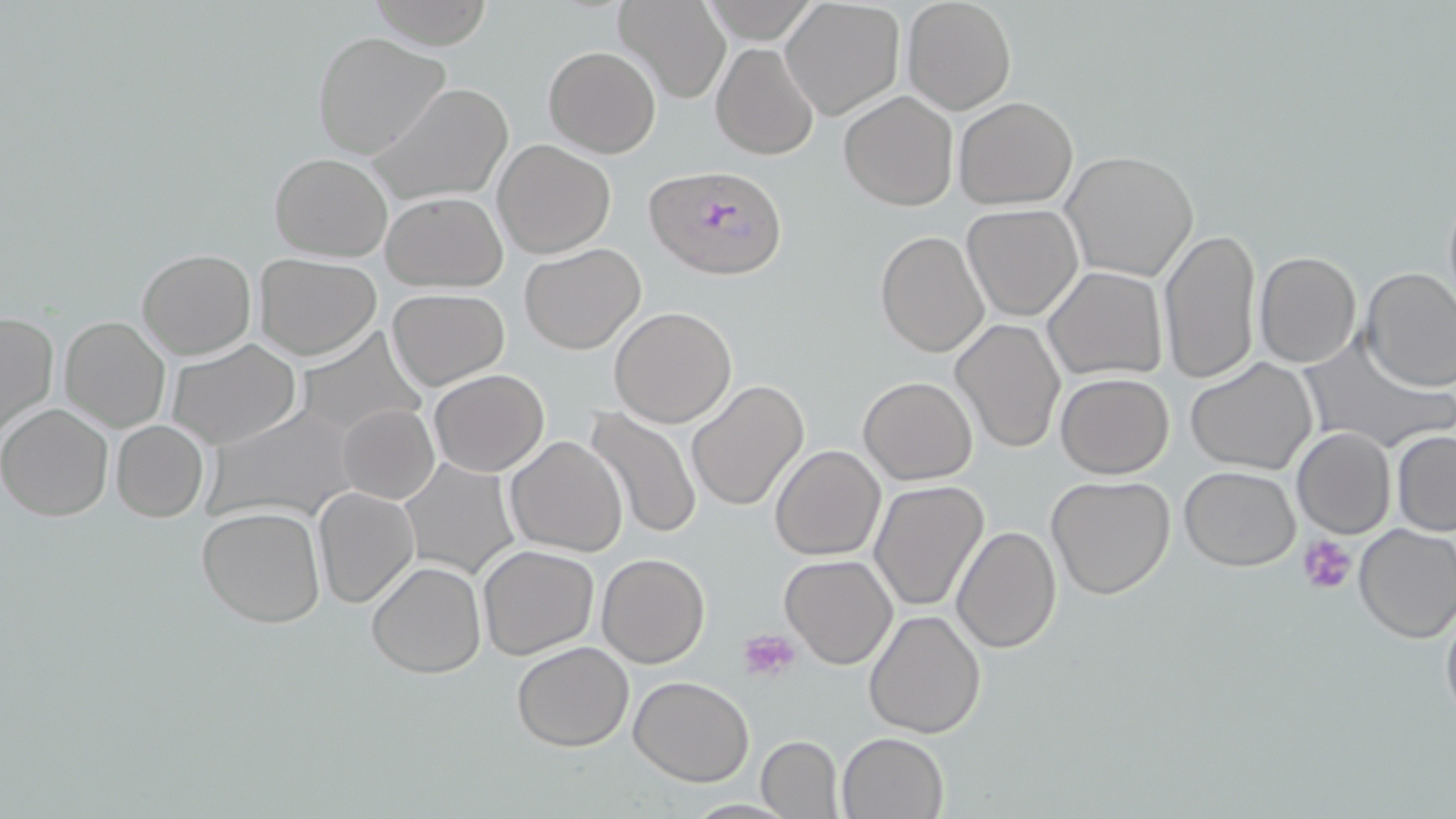 Approximate bounding boxes as (x1, y1, x2, y2) in pixels. Platelet locations: (1298, 534, 1358, 596), (740, 628, 801, 682). Uninfected red blood cell locations: (367, 0, 492, 46), (900, 0, 1016, 114), (613, 2, 729, 105), (781, 2, 907, 120), (312, 30, 449, 159), (711, 42, 819, 161), (544, 45, 661, 158), (369, 81, 515, 205), (839, 91, 958, 210), (953, 96, 1078, 208), (492, 139, 616, 259), (1060, 151, 1199, 282), (270, 152, 392, 262), (1440, 180, 1456, 319), (380, 190, 508, 292), (961, 203, 1083, 322), (1158, 228, 1263, 385), (875, 229, 990, 360), (519, 243, 647, 353), (137, 248, 255, 360), (1253, 250, 1361, 368), (252, 253, 381, 359), (1272, 258, 1451, 379), (1042, 266, 1166, 381), (1359, 266, 1456, 392), (387, 288, 509, 390), (609, 307, 737, 428), (0, 310, 58, 440), (59, 316, 171, 434), (950, 319, 1066, 453), (293, 327, 425, 437), (1297, 334, 1451, 453), (167, 340, 301, 450), (1184, 356, 1320, 475), (428, 369, 548, 476), (1055, 373, 1174, 478), (859, 376, 977, 484), (687, 381, 810, 511), (0, 402, 114, 522), (197, 404, 363, 526), (337, 404, 438, 503), (586, 406, 702, 540), (111, 419, 208, 521), (1292, 427, 1395, 539), (1391, 430, 1456, 537), (505, 435, 629, 558), (771, 444, 886, 561), (400, 458, 520, 579), (1179, 466, 1301, 571), (1046, 474, 1177, 600), (870, 480, 990, 614), (314, 485, 421, 609), (197, 507, 327, 629), (1352, 523, 1456, 643), (952, 524, 1062, 653), (477, 544, 601, 660), (596, 552, 711, 668), (780, 554, 897, 669), (367, 559, 486, 678), (1440, 592, 1456, 733), (864, 608, 986, 739), (512, 641, 634, 751), (628, 676, 754, 785), (836, 730, 948, 818), (755, 735, 844, 819), (678, 797, 804, 817). Plasmodium falciparum-infected red blood cell locations: (645, 164, 788, 279). Slide-level diagnosis: Plasmodium falciparum. Light microscopy. May-Grünwald-Giemsa-stained preparation. Captured at 1000x magnification. Thin blood film. One field of a larger specimen. Image is 1456×819 pixels.